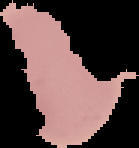

Summary:
  - Image size: 139×148 pixels
  - Preparation: thin blood smear
  - Image type: segmented cell region on a black background
  - Malaria status: uninfected